Outline each Plasmodium falciparum parasite and classify it by life-cycle stage.
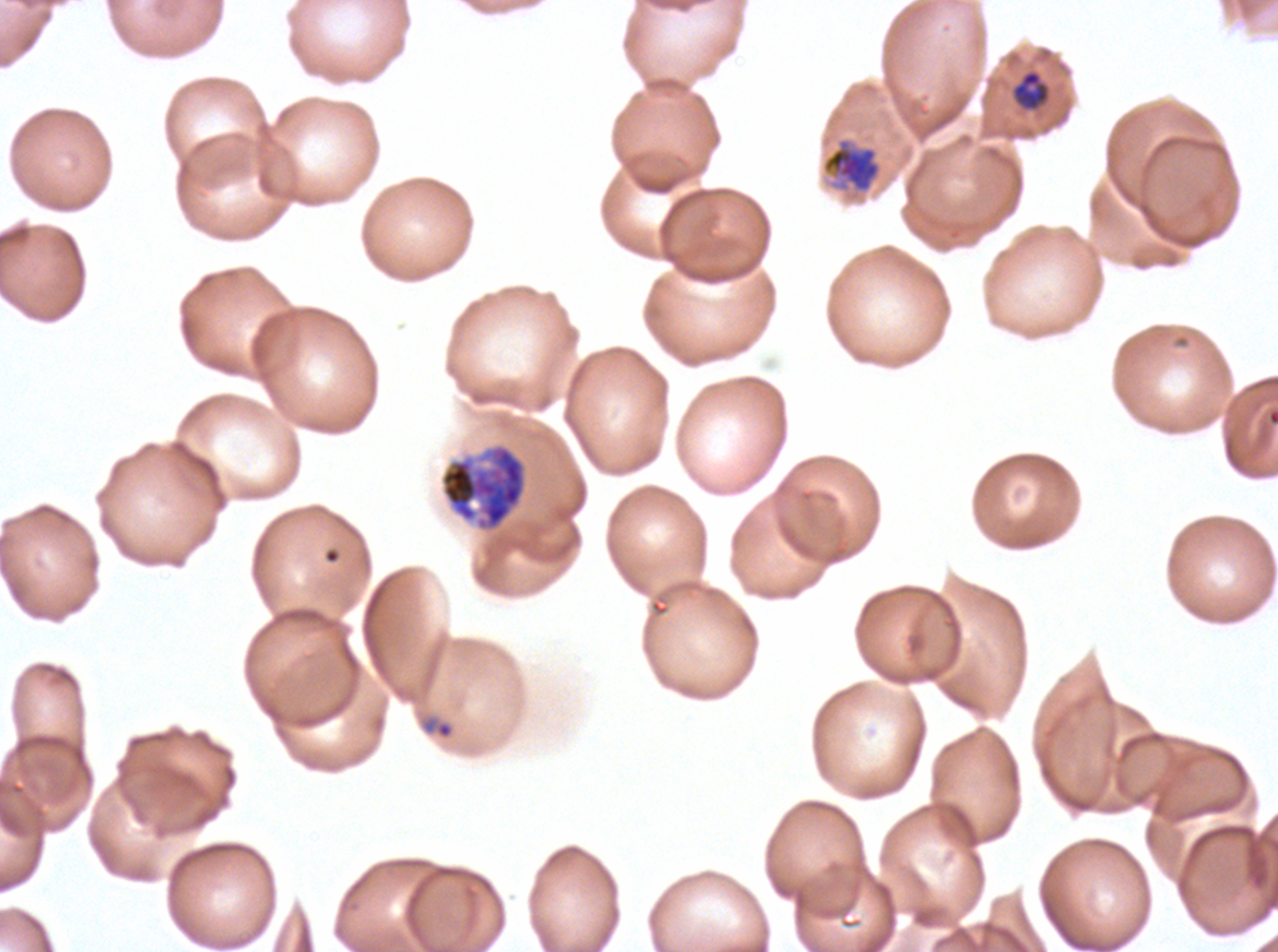
Approximate bounding boxes as {x1, y1, x2, y2} in pixels.
Rings: {422, 716, 455, 739}.
Late-ring/early-trophozoite forms: {1012, 69, 1050, 111}.
Late trophozoites: {822, 139, 881, 192}.
Early schizonts: {439, 442, 528, 532}.
No mid trophozoites, late schizonts, segmenters, or gametocytes observed.

Ex-vivo Plasmodium falciparum culture from a patient in The Gambia, grown for 24 to 48 hours. Thin blood film. Image is 1278×952 pixels. A sub-image separated from a larger composite. Life-cycle stages observed: ring, late-ring/early-trophozoite, late trophozoite, early schizont. Giemsa stain.